Classify this cell by malaria status.
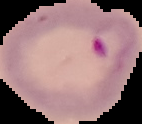

It is parasitized.

From a thin blood film. Segmented cell region on a black background. Image is 142×124 pixels.